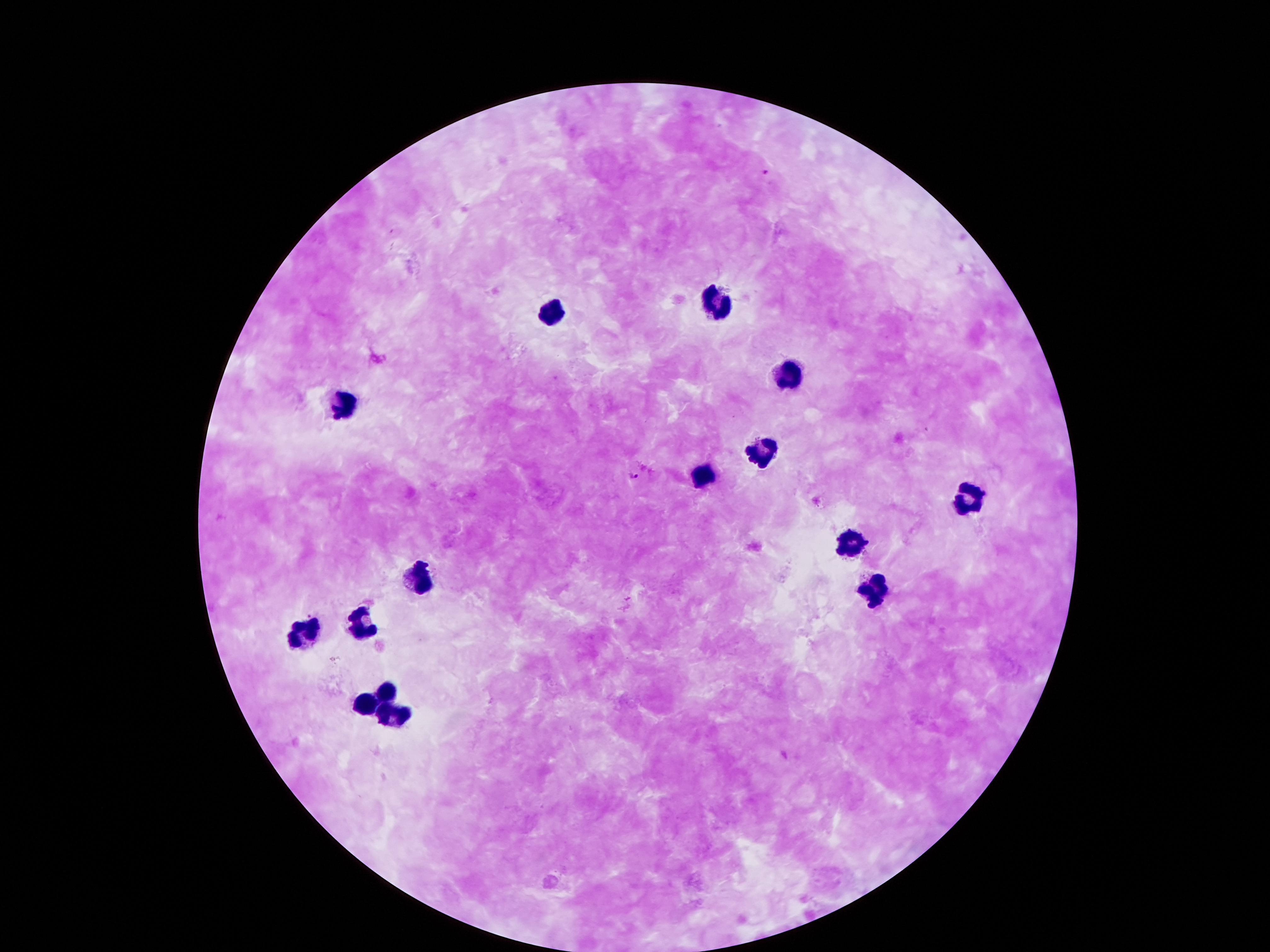
Approximate centers as [x, y] in pixels.
Summary:
  - Leukocyte locations: [710, 305], [554, 315], [789, 369], [344, 405], [766, 453], [699, 478], [965, 495], [850, 546], [422, 574], [873, 593], [366, 624], [307, 630], [386, 686], [366, 704], [394, 711]
  - Plasmodium parasite locations: [765, 172], [635, 477]
  - Patient malaria status: positive for Plasmodium falciparum
  - Image size: 1270×952 pixels
  - Capture: smartphone camera through the microscope eyepiece
  - Magnification: 100x
  - Stain: Giemsa
  - Preparation: thick blood film
  - Field of view: one from this slide